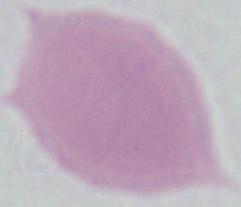 Micrograph. A red blood cell is seen. Captured at 1000x magnification.